Locate every Plasmodium ovale-infected red blood cell.
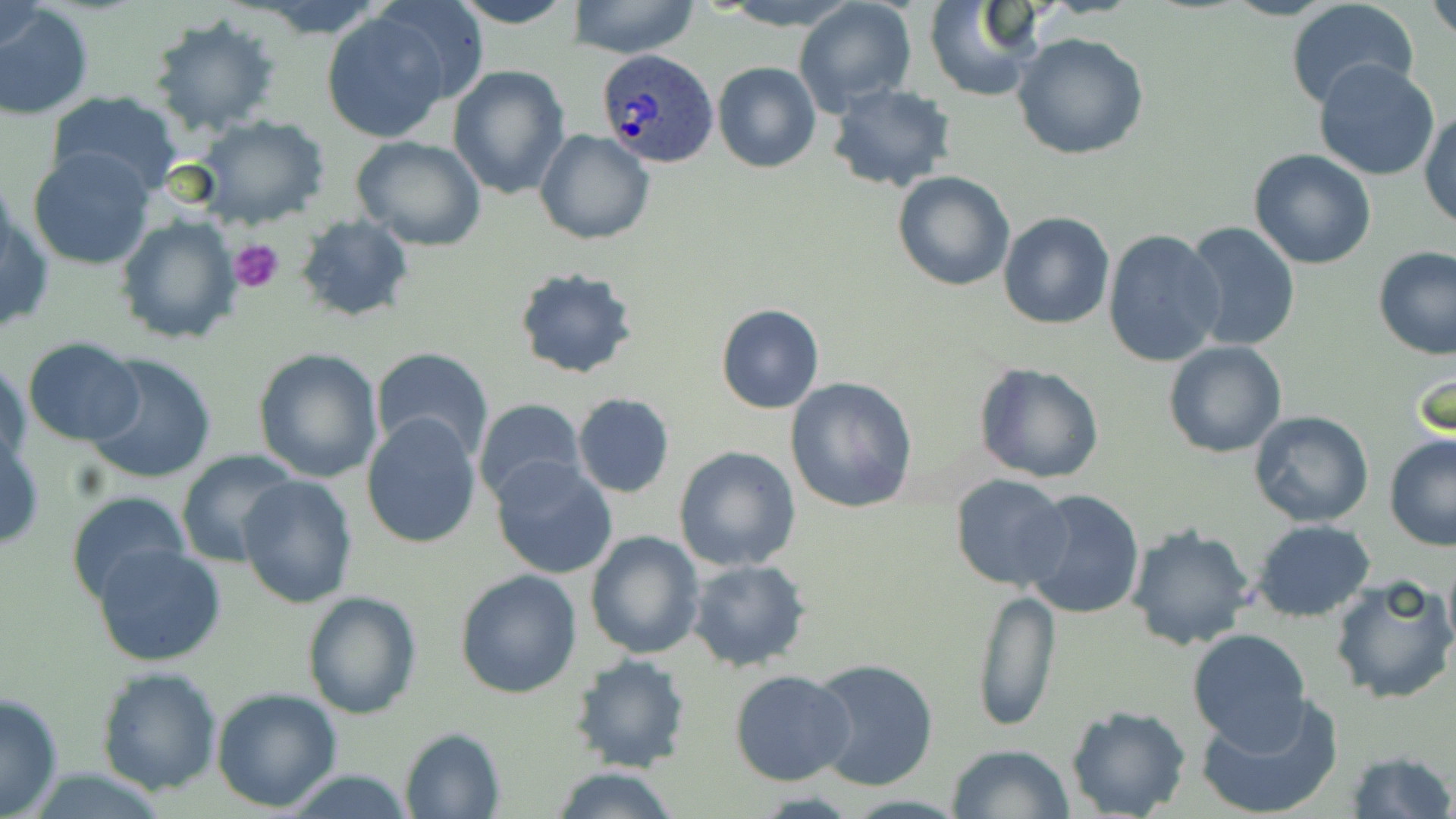

Approximate bounding boxes as (x1,y1)-(x2,y2) corner pairs in pixels.
Plasmodium ovale-infected red blood cells: (597,50)-(717,169).

Platelet locations: (228,236)-(284,292). Uninfected red blood cell locations: (370,0)-(489,105), (450,0)-(578,29), (1426,0)-(1456,40), (570,1)-(701,58), (715,1)-(862,30), (793,1)-(916,116), (923,1)-(1040,101), (2,2)-(47,58), (1287,2)-(1421,113), (250,3)-(388,38), (0,4)-(94,119), (319,10)-(453,143), (146,15)-(281,136), (1012,31)-(1148,160), (1313,59)-(1441,181), (713,61)-(821,173), (447,64)-(570,199), (828,83)-(956,192), (46,89)-(182,195), (1420,106)-(1455,230), (194,114)-(330,228), (534,129)-(655,244), (351,135)-(487,250), (27,148)-(157,271), (1248,149)-(1377,269), (893,172)-(1016,292), (2,198)-(53,341), (998,211)-(1115,329), (116,214)-(241,344), (295,214)-(415,323), (1184,221)-(1300,355), (1102,228)-(1226,369), (1374,247)-(1456,362), (513,267)-(639,381), (716,304)-(823,414), (22,338)-(145,445), (1163,341)-(1288,458), (371,346)-(494,464), (253,348)-(383,483), (83,352)-(218,486), (1,360)-(30,474), (1409,360)-(1453,449), (974,362)-(1104,484), (784,377)-(917,513), (572,392)-(675,498), (472,397)-(586,503), (1247,411)-(1374,528), (361,413)-(483,550), (1385,434)-(1456,551), (0,435)-(45,553), (673,446)-(800,572), (177,449)-(300,568), (490,455)-(619,580), (239,475)-(357,609), (950,477)-(1073,590), (1019,488)-(1145,620), (65,490)-(193,607), (1251,518)-(1377,622), (1127,525)-(1255,651), (585,529)-(705,661), (92,544)-(228,666), (1441,554)-(1455,660), (686,559)-(811,671), (454,568)-(583,698), (1328,575)-(1456,707), (971,586)-(1061,732), (301,591)-(421,719), (1186,629)-(1313,750), (568,654)-(693,774), (807,657)-(940,793), (95,666)-(223,794), (729,670)-(856,786), (212,687)-(343,810), (0,691)-(65,819), (1195,694)-(1343,819), (1065,705)-(1191,819), (400,727)-(506,818), (947,742)-(1075,819), (1344,751)-(1454,819), (549,765)-(682,819), (278,770)-(419,818). Slide-level diagnosis: Plasmodium ovale. Thin blood film. Light microscopy. Captured at 1000x magnification. One field of a larger specimen. Image is 1456×819 pixels. May-Grünwald-Giemsa-stained preparation.